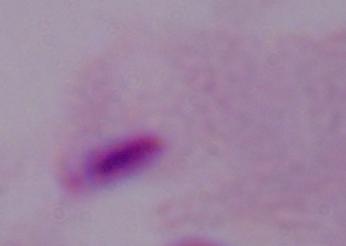

magnification: 1000x
identification: trichomonad
modality: micrograph